Assess the morphology of the erythrocytes.
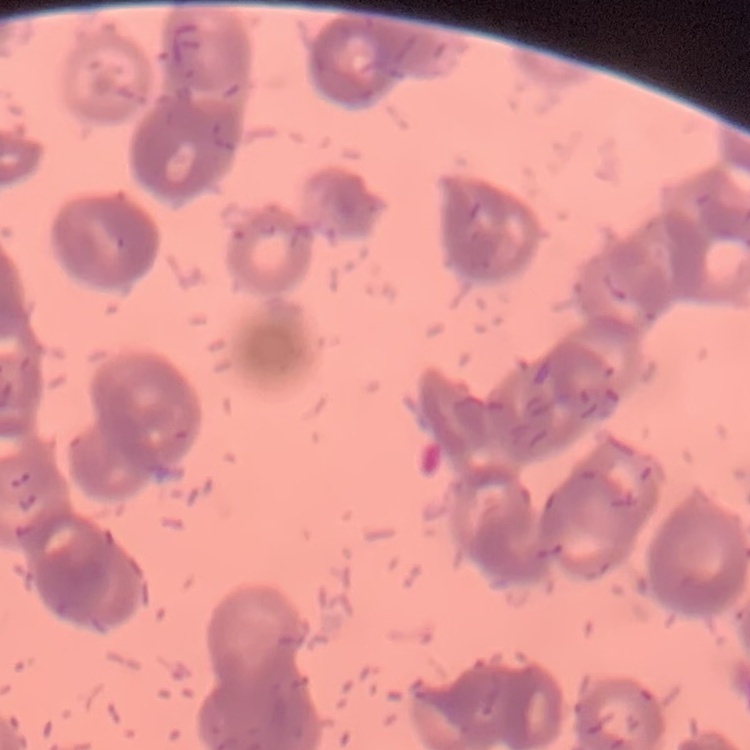
They show rouleaux formation.

Summary:
  - Preparation: thin blood film
  - Stain: Field's or Giemsa
  - Image type: square crop of a larger photomicrograph